Comment on the morphology of the erythrocytes.
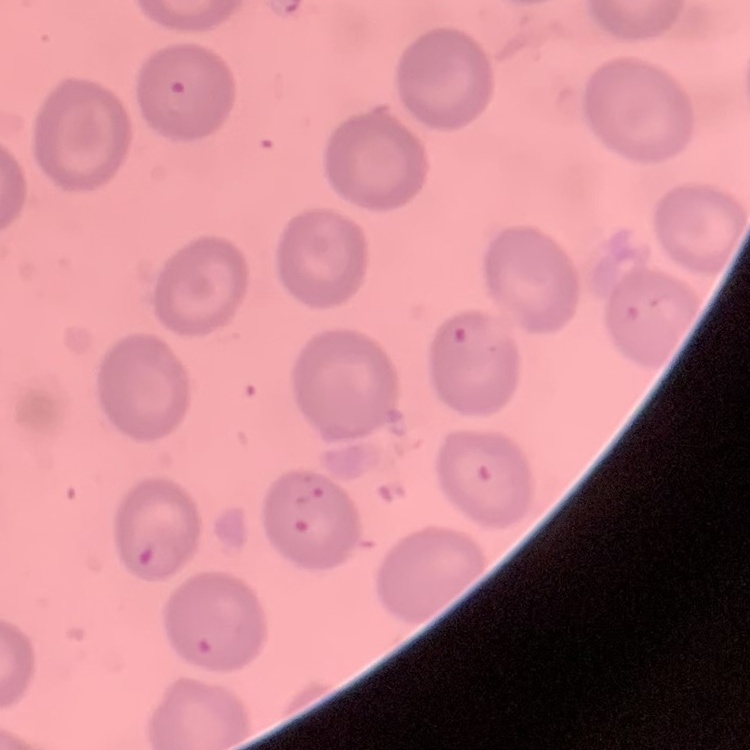
No rouleaux formation.

{
  "image_type": "one tile cut from a larger photomicrograph",
  "preparation": "thin peripheral smear",
  "stain": "Field's or Giemsa"
}